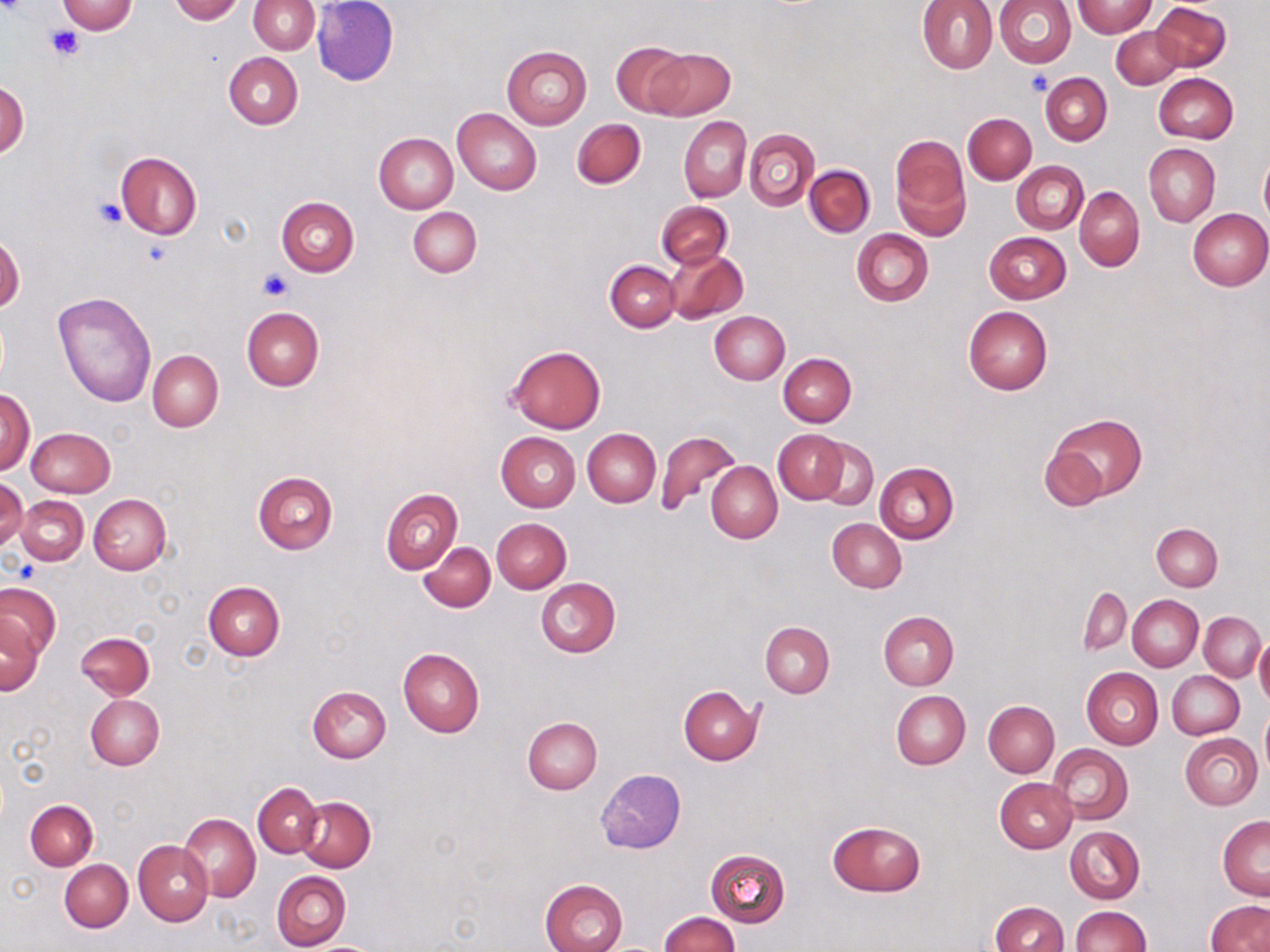

slide-level diagnosis = no evidence of blood parasites
stain = May-Grünwald-Giemsa
modality = optical microscopy
magnification = 1000x
field of view = single
image size = 1270×952 pixels
platelet locations = approximate bounding boxes as [x1, y1, x2, y2] in pixels: [45, 25, 84, 61], [1023, 69, 1052, 97], [94, 198, 126, 228], [259, 268, 291, 300], [10, 561, 37, 582]
uninfected red blood cell locations = approximate bounding boxes as [x1, y1, x2, y2] in pixels: [57, 0, 136, 34], [239, 0, 313, 129], [312, 0, 398, 86], [917, 0, 997, 73], [993, 0, 1077, 67], [170, 1, 245, 23], [248, 1, 319, 54], [1072, 1, 1157, 37], [1152, 2, 1232, 72], [1110, 26, 1183, 89], [611, 41, 694, 117], [502, 46, 592, 129], [647, 47, 734, 121], [223, 52, 303, 129], [1040, 71, 1111, 145], [1154, 72, 1238, 143], [0, 78, 29, 159], [452, 107, 541, 195], [963, 113, 1036, 184], [678, 116, 751, 202], [572, 119, 645, 188], [744, 130, 819, 210], [374, 131, 459, 212], [890, 137, 969, 238], [1144, 143, 1220, 227], [115, 151, 202, 239], [1259, 155, 1270, 227], [1012, 161, 1089, 234], [804, 165, 874, 237], [1074, 186, 1145, 271], [276, 196, 359, 277], [658, 201, 733, 268], [409, 207, 482, 277], [1187, 208, 1270, 290], [852, 228, 933, 306], [983, 232, 1071, 303], [1, 233, 24, 314], [665, 249, 749, 324], [605, 260, 679, 332], [51, 291, 157, 407], [964, 305, 1053, 395], [241, 307, 323, 390], [710, 311, 790, 384], [507, 345, 605, 434], [148, 350, 223, 432], [778, 352, 856, 427], [1, 387, 35, 476], [1046, 413, 1145, 504], [25, 427, 115, 496], [583, 429, 660, 506], [774, 429, 848, 505], [656, 431, 740, 517], [496, 432, 581, 512], [816, 439, 879, 509], [1036, 444, 1111, 512], [705, 462, 782, 543], [875, 463, 959, 543], [253, 471, 338, 553], [0, 477, 28, 550], [380, 488, 463, 574], [89, 494, 172, 575], [17, 495, 89, 565], [491, 518, 572, 593], [827, 518, 906, 593], [1152, 524, 1222, 591], [419, 542, 495, 612], [535, 577, 620, 657], [0, 583, 60, 660], [203, 583, 284, 660], [1078, 586, 1131, 656], [1127, 594, 1203, 670], [878, 611, 958, 690], [1200, 611, 1265, 681], [1, 615, 44, 697], [760, 622, 835, 697], [77, 631, 155, 699], [1254, 636, 1270, 711], [397, 649, 484, 737], [1081, 667, 1163, 749], [1168, 671, 1244, 739], [678, 685, 762, 764], [308, 687, 391, 763], [891, 690, 970, 770], [84, 695, 164, 770], [983, 701, 1059, 777], [1259, 709, 1270, 780], [522, 717, 602, 794], [1179, 732, 1262, 810], [1047, 745, 1132, 825], [596, 769, 687, 854], [996, 778, 1076, 853], [252, 782, 322, 858], [296, 796, 375, 871], [25, 800, 98, 870], [179, 813, 260, 900], [1217, 815, 1270, 899], [828, 820, 925, 896], [1065, 825, 1145, 904], [133, 841, 213, 926], [706, 849, 790, 926], [60, 859, 132, 932], [272, 870, 351, 950], [539, 879, 627, 952], [1206, 900, 1270, 952], [989, 902, 1067, 952], [1070, 906, 1150, 952], [660, 912, 739, 952]
preparation = thin blood film